Locate every Babesia divergens-infected red blood cell.
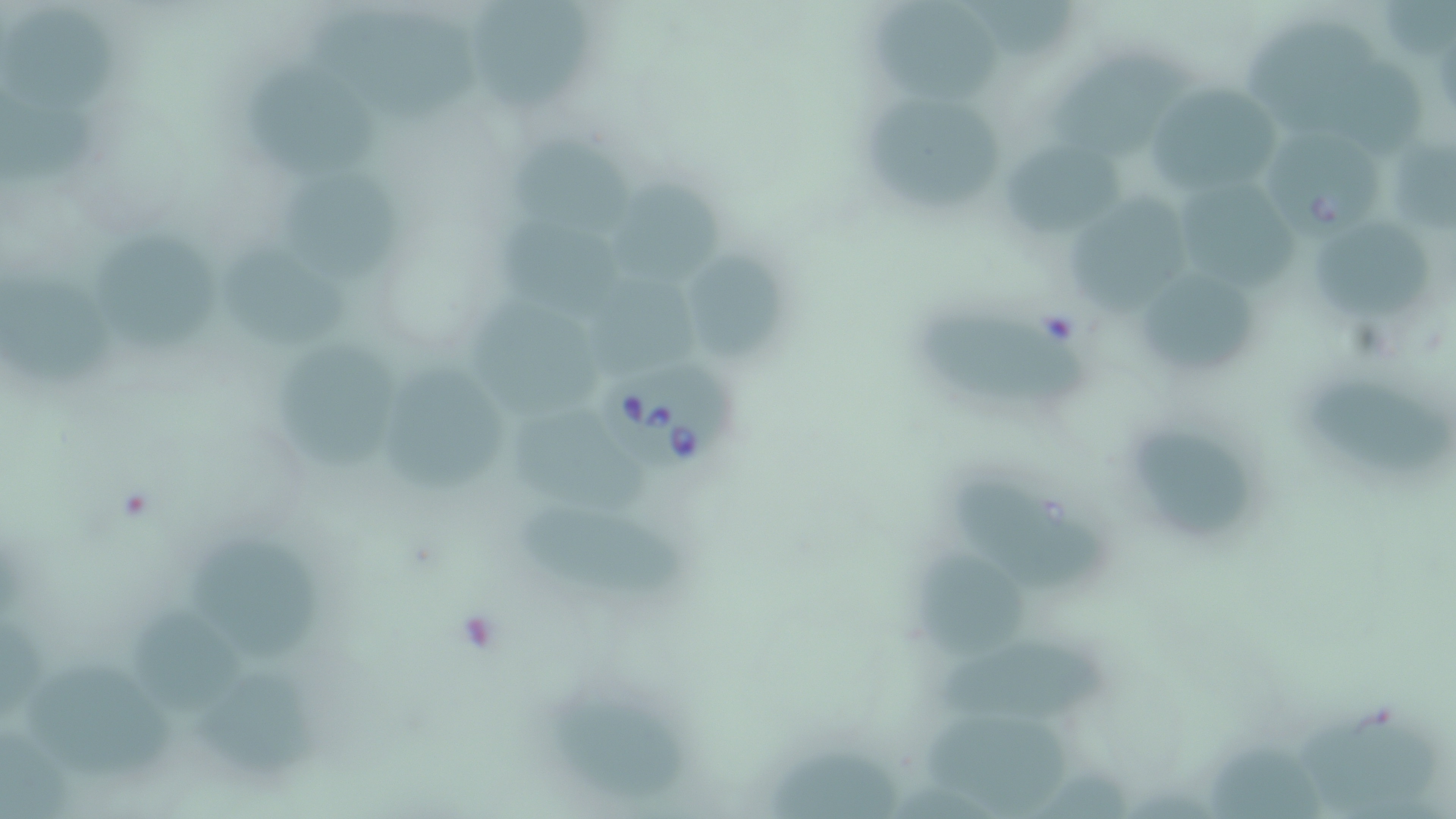

Approximate bounding boxes as [x1, y1, x2, y2] in pixels.
Babesia divergens-infected red blood cells: [1268, 129, 1389, 247], [597, 362, 742, 473].

slide-level diagnosis = Babesia divergens
magnification = 1000x
modality = light microscopy
stain = May-Grünwald-Giemsa
uninfected red blood cell locations = approximate bounding boxes as [x1, y1, x2, y2] in pixels: [871, 1, 1008, 98], [467, 5, 595, 117], [0, 6, 115, 119], [309, 6, 484, 122], [1240, 20, 1377, 126], [1050, 47, 1196, 159], [251, 64, 386, 182], [1148, 83, 1288, 200], [875, 95, 1000, 216], [1388, 129, 1456, 238], [506, 137, 639, 241], [999, 143, 1127, 241], [285, 164, 400, 290], [603, 179, 730, 286], [1185, 179, 1306, 288], [1067, 193, 1202, 315], [493, 216, 627, 318], [1312, 220, 1439, 326], [97, 229, 222, 353], [217, 243, 355, 352], [685, 253, 786, 358], [1132, 268, 1259, 374], [7, 271, 116, 386], [590, 272, 713, 376], [464, 293, 612, 416], [910, 303, 1095, 409], [273, 342, 411, 469], [382, 366, 509, 497], [1304, 386, 1452, 479], [506, 403, 659, 509], [1122, 418, 1263, 546], [951, 462, 1112, 600], [523, 503, 696, 599], [195, 536, 333, 665], [921, 544, 1034, 654], [134, 607, 245, 719], [926, 628, 1114, 723], [26, 653, 177, 778], [196, 667, 323, 777], [550, 690, 692, 798], [1297, 704, 1436, 819], [919, 705, 1066, 819], [1210, 739, 1331, 819], [770, 742, 899, 819]
image size = 1456×819 pixels
field of view = single
preparation = thin blood smear